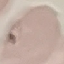

Summary:
  - Result: no malaria parasites detected
  - Stain: Giemsa
  - Capture: smartphone through the microscope eyepiece
  - Image type: cell patch, automatically extracted from a larger field of view and resized to 64 × 64 pixels
  - Preparation: thin smear